Outline each blood parasite and name the species.
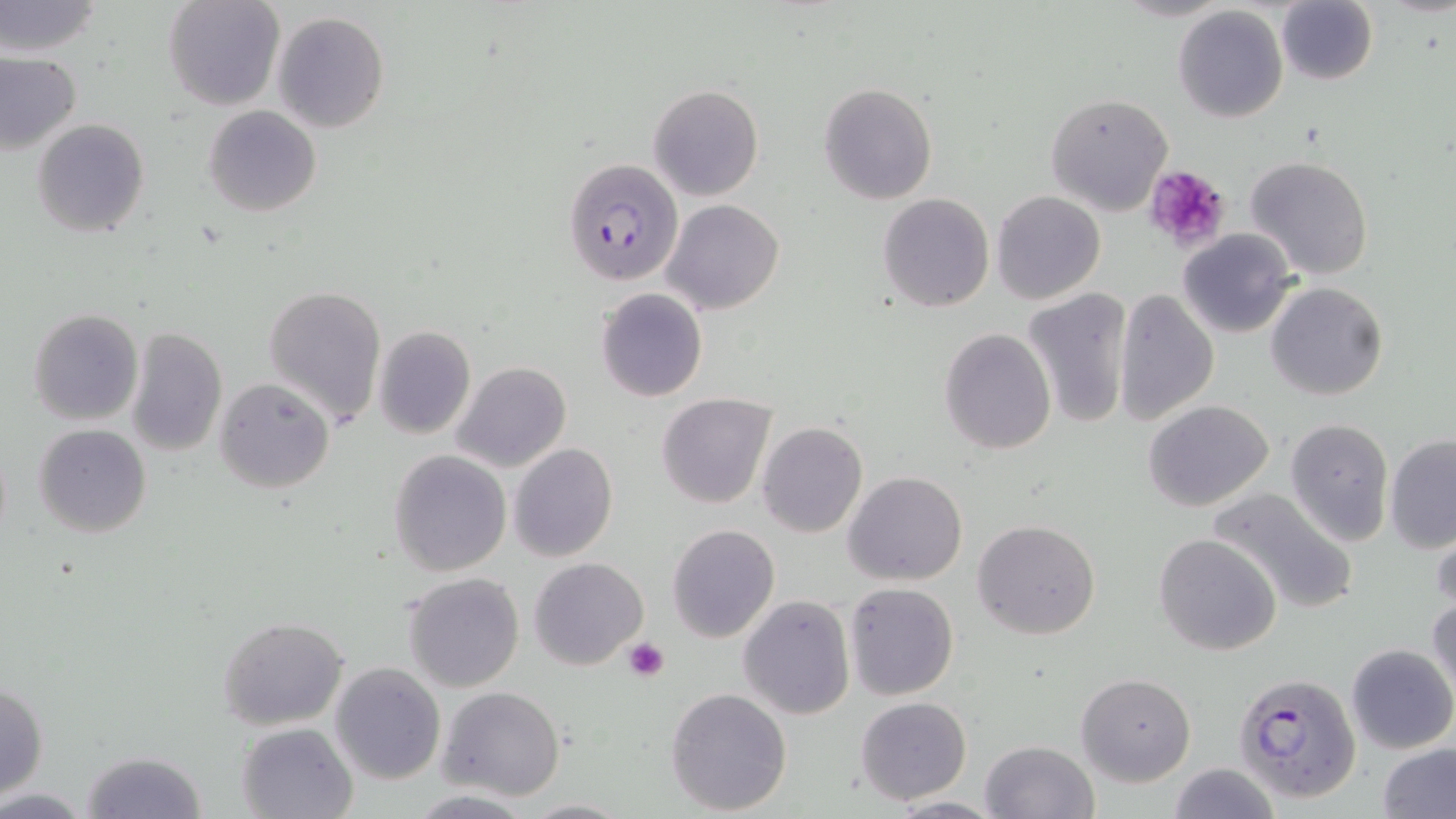
Approximate bounding boxes as (x1,y1)-(x2,y2) corner pairs in pixels.
Plasmodium falciparum-infected red blood cells: (563,158)-(684,287), (1234,671)-(1362,803).
No Plasmodium ovale, Plasmodium malariae, Plasmodium vivax, Babesia divergens, or Trypanosoma brucei observed.

Summary:
  - Uninfected red blood cell locations: (0,0)-(105,59), (162,0)-(285,111), (1276,1)-(1377,84), (1172,6)-(1289,124), (272,11)-(390,134), (0,51)-(81,155), (819,82)-(937,205), (647,84)-(763,201), (1046,93)-(1173,215), (203,105)-(321,218), (33,119)-(152,238), (1246,155)-(1372,281), (992,191)-(1106,306), (877,193)-(994,312), (662,199)-(784,315), (1177,229)-(1297,339), (1266,281)-(1387,400), (261,285)-(387,425), (595,288)-(707,402), (1113,288)-(1220,426), (1021,289)-(1133,431), (27,307)-(143,425), (123,325)-(226,457), (374,326)-(476,438), (938,328)-(1056,455), (452,361)-(571,473), (215,377)-(336,494), (656,393)-(777,508), (1143,400)-(1275,512), (1285,418)-(1394,545), (756,421)-(868,537), (33,424)-(151,537), (1384,435)-(1456,553), (508,443)-(618,562), (389,450)-(510,577), (843,472)-(967,587), (1206,485)-(1362,616), (1429,517)-(1455,613), (974,519)-(1100,640), (666,523)-(780,643), (1154,533)-(1282,656), (530,557)-(648,670), (403,572)-(524,692), (845,582)-(959,700), (1427,593)-(1456,706), (738,596)-(855,720), (217,616)-(348,729), (1346,644)-(1456,753), (330,663)-(445,783), (1077,671)-(1196,785), (0,683)-(49,796), (436,686)-(564,800), (665,686)-(792,815), (855,697)-(972,805), (236,721)-(359,819), (980,739)-(1098,819), (1379,745)-(1456,819), (78,750)-(208,819), (1166,763)-(1279,819), (885,795)-(1004,817), (517,798)-(633,817)
  - Platelet locations: (1142,164)-(1233,253), (623,637)-(670,682)
  - Slide-level diagnosis: Plasmodium falciparum
  - Image size: 1456×819 pixels
  - Modality: light microscopy
  - Magnification: 1000x
  - Field of view: one of a larger specimen
  - Preparation: thin blood smear
  - Stain: May-Grünwald-Giemsa